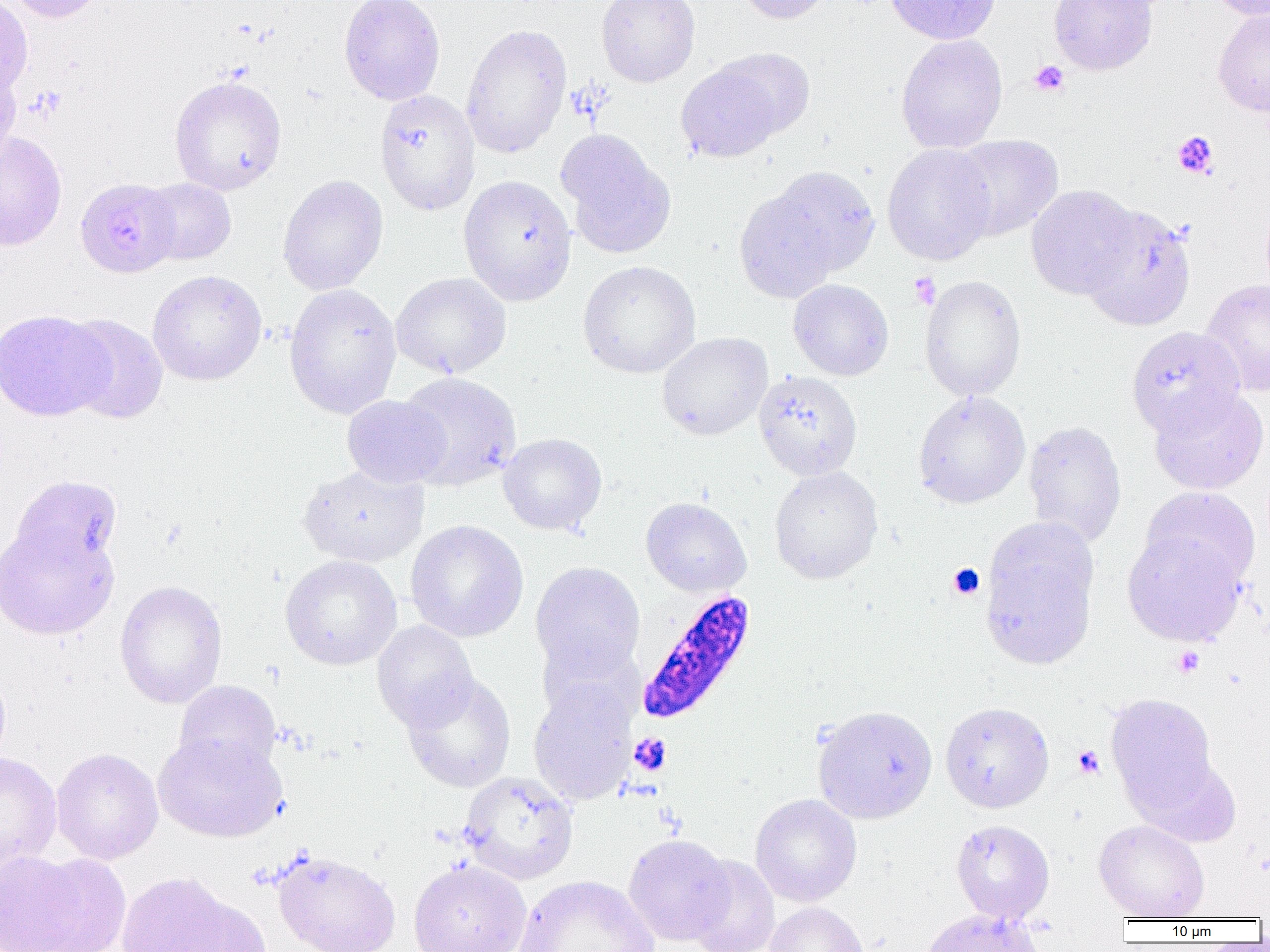

slide-level diagnosis = Plasmodium falciparum
modality = optical microscopy
preparation = thin blood smear
platelet locations = approximate bounding boxes as (x1, y1, x2, y2) in pixels: (1029, 60, 1069, 96), (26, 88, 66, 123), (1172, 131, 1219, 178), (908, 272, 941, 309), (947, 564, 985, 600), (1172, 646, 1205, 677), (629, 733, 672, 776), (1073, 745, 1104, 778)
uninfected red blood cell locations = approximate bounding boxes as (x1, y1, x2, y2) in pixels: (4, 0, 109, 23), (338, 0, 446, 105), (596, 0, 700, 87), (734, 0, 836, 24), (884, 0, 1000, 45), (1048, 0, 1158, 75), (1207, 0, 1269, 22), (0, 1, 33, 97), (1213, 8, 1270, 117), (461, 23, 572, 159), (896, 34, 1008, 153), (713, 47, 815, 138), (0, 60, 22, 168), (676, 62, 783, 163), (169, 75, 287, 195), (375, 89, 480, 216), (555, 129, 676, 260), (0, 132, 67, 251), (948, 134, 1063, 240), (881, 143, 997, 266), (761, 165, 880, 281), (277, 174, 388, 295), (458, 174, 577, 306), (75, 178, 181, 277), (141, 178, 236, 265), (734, 185, 845, 303), (1025, 185, 1141, 300), (1080, 204, 1196, 331), (578, 260, 700, 378), (147, 269, 267, 385), (390, 272, 511, 379), (919, 274, 1027, 401), (1200, 278, 1270, 397), (788, 279, 894, 381), (284, 283, 402, 419), (0, 309, 112, 421), (61, 313, 169, 423), (1126, 325, 1245, 436), (656, 332, 772, 441), (754, 370, 863, 481), (396, 371, 522, 491), (1148, 385, 1269, 495), (913, 390, 1030, 508), (342, 394, 450, 488), (1022, 421, 1127, 548), (497, 433, 607, 535), (298, 464, 429, 567), (769, 466, 883, 584), (10, 474, 123, 573), (1141, 486, 1261, 588), (640, 497, 752, 597), (405, 520, 528, 642), (0, 521, 119, 640), (980, 524, 1099, 670), (1122, 530, 1247, 645), (280, 554, 402, 670), (530, 562, 645, 680), (114, 580, 228, 709), (372, 620, 479, 731), (538, 637, 645, 730), (401, 673, 517, 793), (173, 679, 282, 777), (528, 679, 638, 804), (1105, 692, 1219, 814), (940, 701, 1054, 813), (812, 705, 937, 823), (153, 732, 287, 842), (51, 748, 163, 864), (0, 751, 62, 878), (1133, 754, 1243, 848), (458, 771, 579, 884), (750, 793, 862, 907), (951, 819, 1055, 923), (1093, 819, 1210, 921), (623, 834, 734, 945), (272, 848, 401, 952), (0, 851, 126, 952), (685, 855, 780, 952), (408, 859, 531, 952), (114, 871, 247, 952), (514, 875, 658, 952), (167, 896, 272, 952), (764, 902, 869, 952), (922, 907, 1043, 952)
image size = 1270×952 pixels
magnification = 1000x
field of view = one of a larger specimen
Plasmodium falciparum-infected red blood cell locations = approximate bounding boxes as (x1, y1, x2, y2) in pixels: (631, 588, 755, 725)